Report the malaria status.
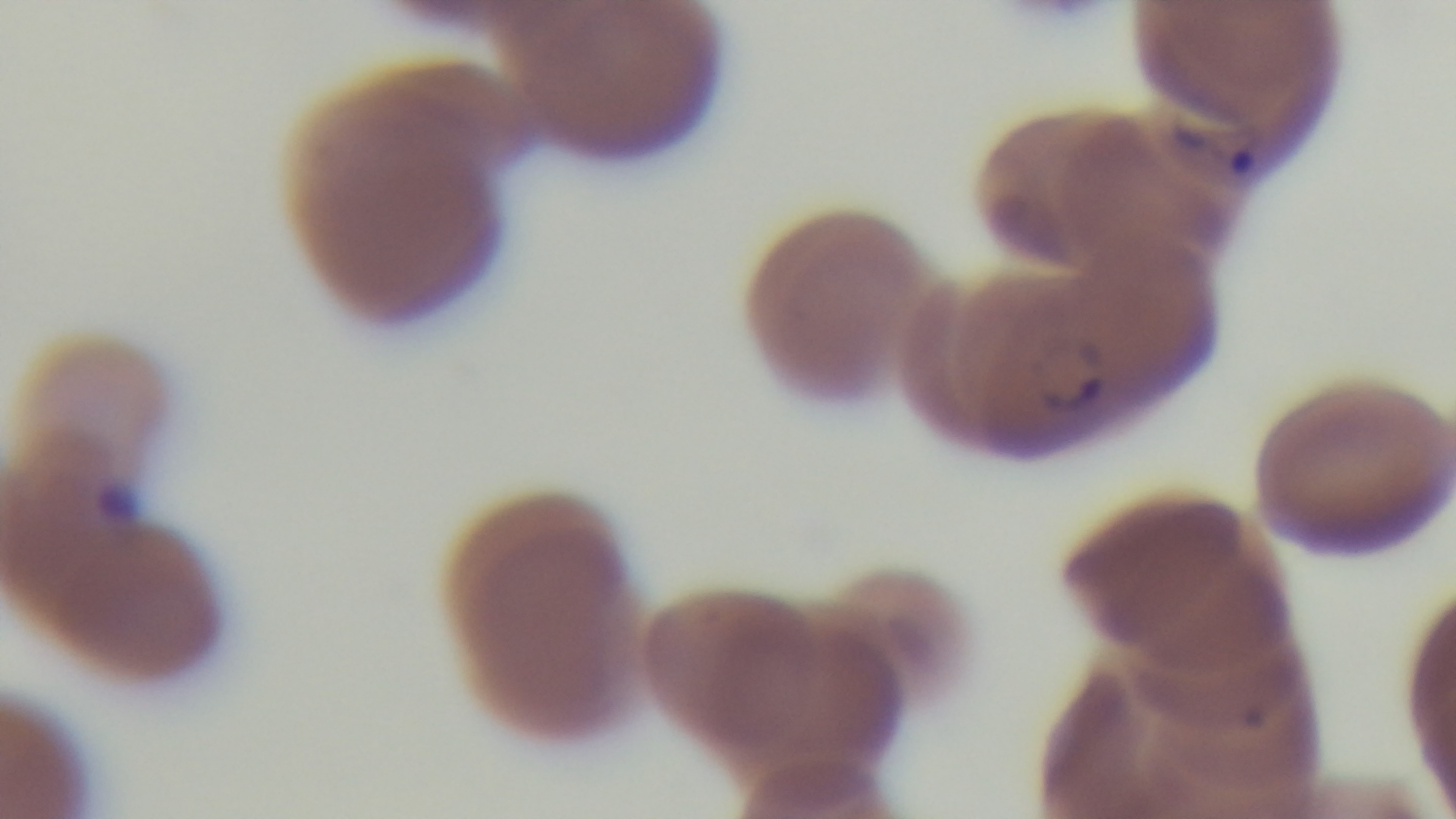

Positive.

Summary:
  - Preparation: thin blood film
  - Modality: light microscopy
  - Objective: 100x oil immersion
  - Capture: mounted 4K digital camera
  - Field of view: single
  - Stain: Giemsa